Classify this cell by malaria status.
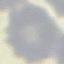

It is uninfected.

Acquired by smartphone through the microscope eyepiece. Thin smear of blood. Automatically extracted cell patch, resized to 64 × 64 pixels. Giemsa-stained preparation.